Point out each leukocyte.
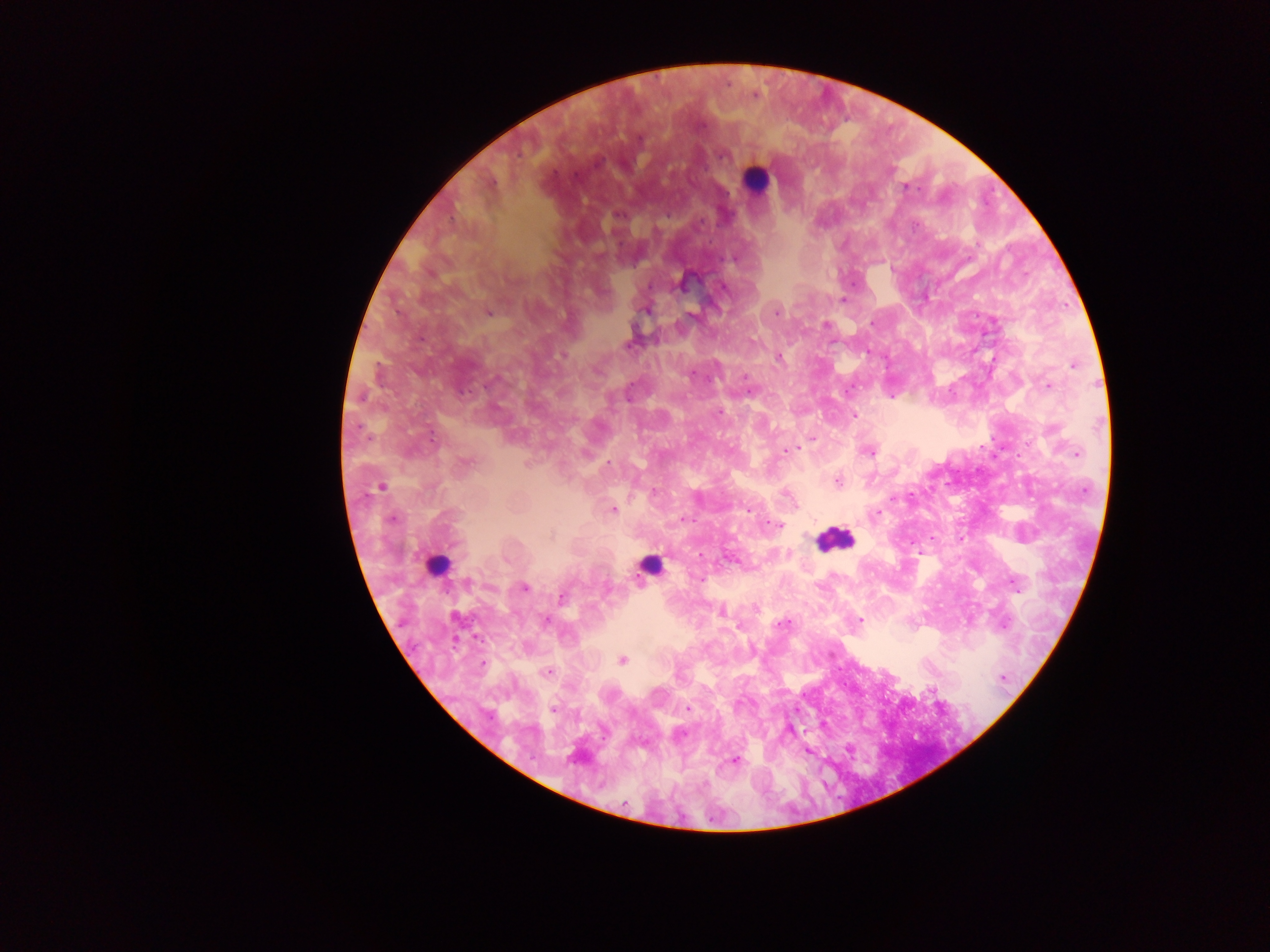
Approximate centers as (x, y) in pixels.
Leukocytes: (755, 180), (832, 538), (436, 565), (651, 566).

capture = mobile-phone photograph through a microscope
Plasmodium parasite locations = approximate centers as (x, y) in pixels: (700, 126), (722, 155), (616, 214), (843, 300), (646, 309), (488, 312), (777, 312), (694, 316), (871, 324), (827, 325), (629, 345), (779, 358), (1074, 365), (691, 374), (745, 377), (1047, 387), (750, 391), (719, 412), (854, 415), (812, 437), (787, 451), (869, 453), (1077, 453), (468, 462), (608, 463), (837, 481), (381, 486), (786, 493), (613, 510), (748, 510), (877, 514), (391, 519), (683, 519), (778, 525), (699, 579), (468, 581), (523, 588), (562, 597), (722, 611), (546, 620), (859, 620), (783, 624), (623, 660), (483, 664), (547, 671), (1003, 677), (687, 708), (553, 710), (734, 761)
image size = 1270×952 pixels
country = Ghana
preparation = thick blood smear
field of view = single